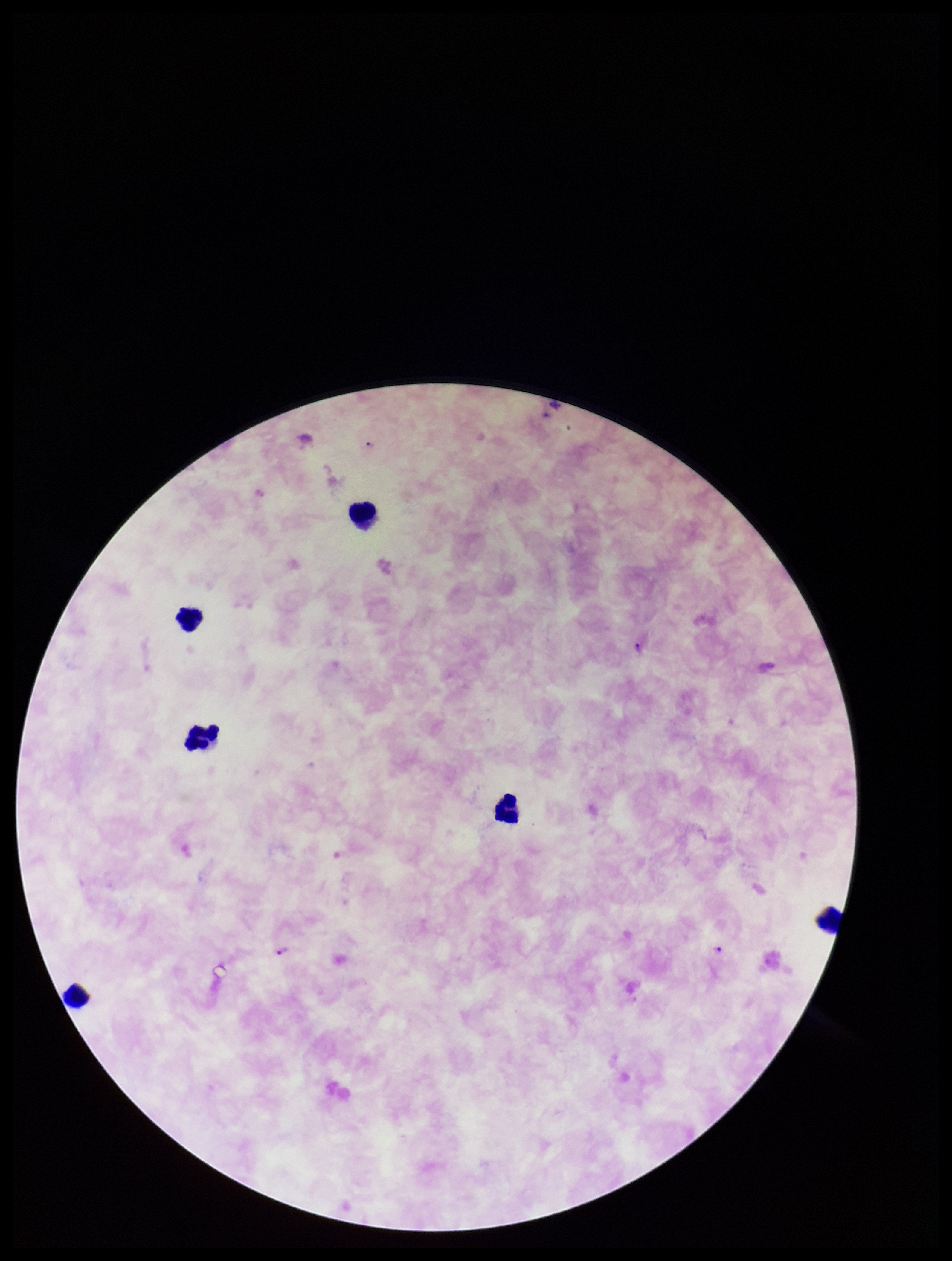 Single field of view. Plasmodium parasites: seen. Patient malaria status: infected. Stained with Giemsa. Species reported for this patient: Plasmodium falciparum. Image is 952×1261 pixels. Parasite count: 1. Photographed through the microscope eyepiece with a smartphone camera. Preparation: thick smear. Leukocyte count: 6.